State the preparation type.
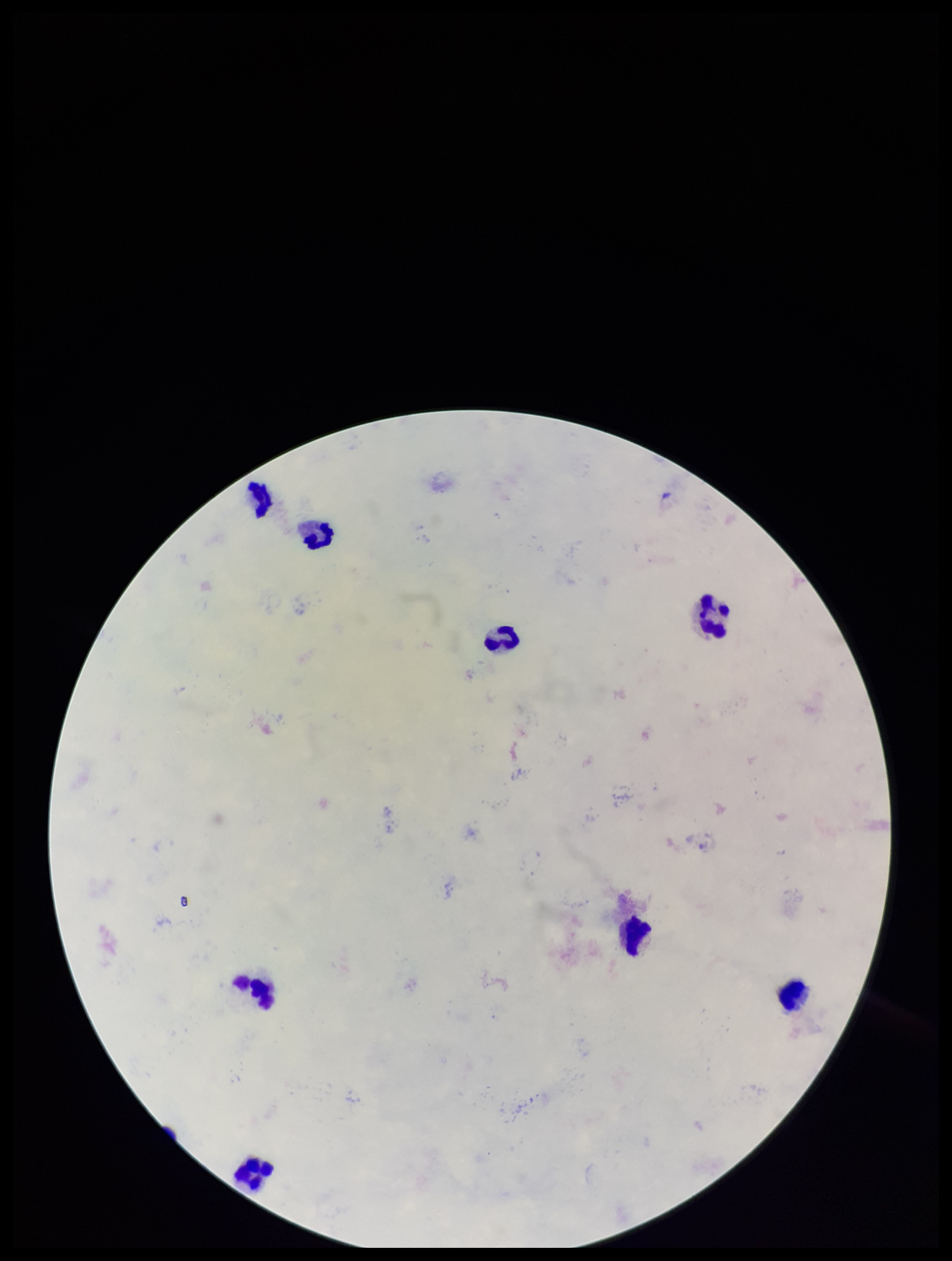
Thick.

Photographed through the microscope eyepiece with a smartphone camera. Single field of view. Patient malaria status: negative. Parasite count: 0. Plasmodium parasites: none detected. Image is 952×1261 pixels. Giemsa stain. Leukocyte count: 8.